Find the red blood cells and label each as Plasmodium falciparum-infected, uninfected, or of indeterminate infection status.
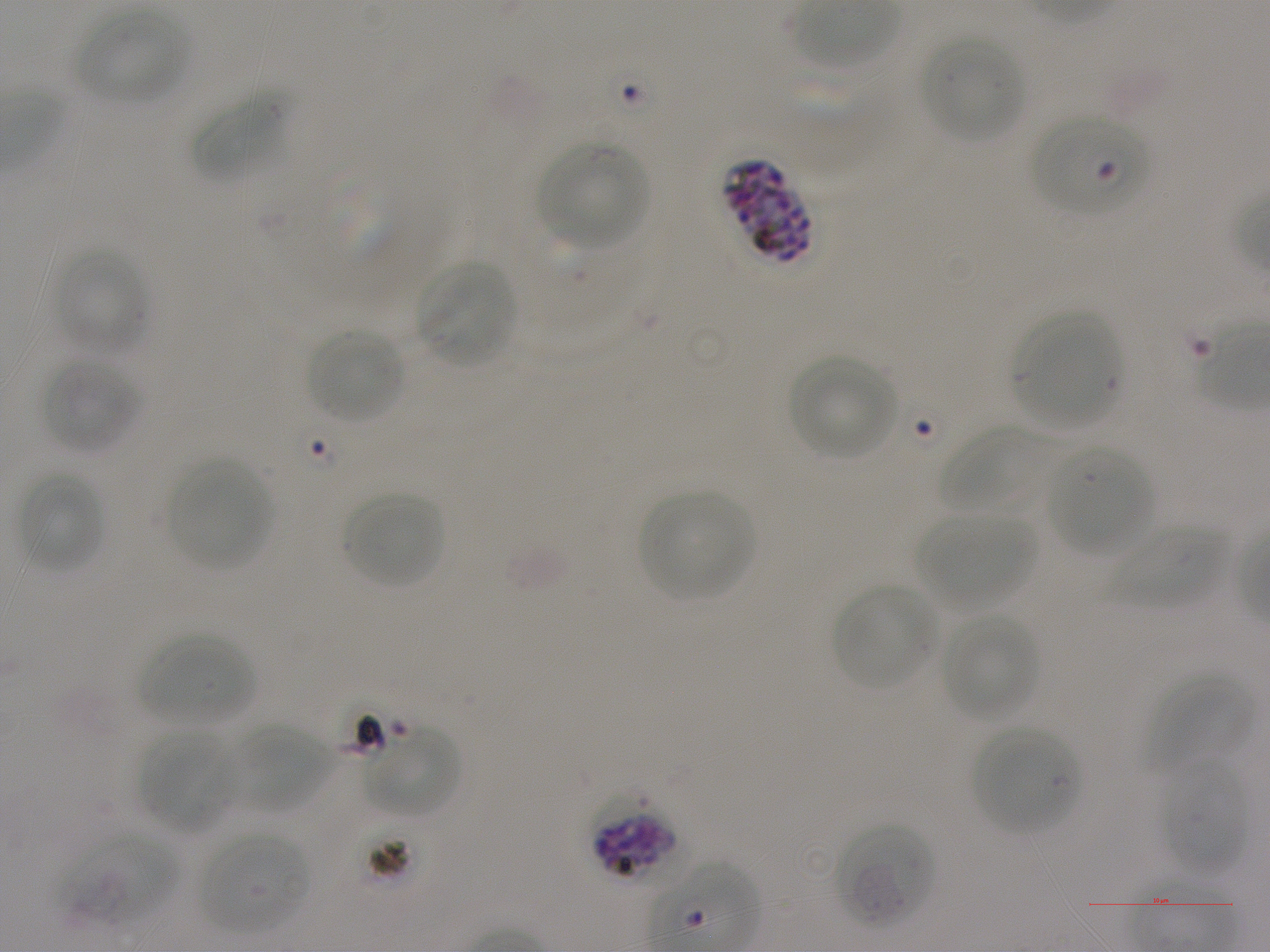

Approximate bounding boxes as [x1, y1, x2, y2] in pixels. Not every red blood cell is marked. A life-cycle stage — or a range of stages, where the recorded stages span more than one — follows each staged infected red blood cell.
Infected red blood cells: [1031, 115, 1151, 217] early ring; [725, 160, 814, 264] late schizont; [588, 793, 680, 882] schizont.
Red blood cells of indeterminate infection status: [56, 829, 178, 930].
Uninfected red blood cells: [77, 8, 187, 105], [920, 32, 1024, 142], [192, 92, 288, 183], [537, 142, 650, 247], [50, 245, 151, 354], [414, 260, 518, 367], [1012, 310, 1121, 431], [305, 329, 403, 424], [787, 355, 898, 460], [41, 356, 139, 453], [939, 425, 1057, 518], [1045, 444, 1153, 555], [165, 458, 270, 570], [17, 471, 106, 573], [638, 490, 755, 601], [341, 491, 445, 589], [918, 511, 1035, 611], [1109, 524, 1230, 609], [832, 584, 939, 691], [939, 613, 1040, 722], [139, 631, 255, 729], [1150, 674, 1254, 772], [232, 721, 332, 813], [364, 725, 460, 818], [971, 726, 1080, 835], [140, 730, 237, 832], [1158, 759, 1247, 877], [833, 822, 936, 929], [197, 832, 311, 935].

Summary:
  - Donor blood group: A+
  - Life-cycle stages observed: ring, schizont
  - Objective: 100x, oil immersion, numerical aperture 1.25
  - Stain: Giemsa
  - Culture: in-vitro Plasmodium falciparum strain NF54, static
  - Preparation: thin blood smear
  - Field of view: single
  - Image size: 1270×952 pixels